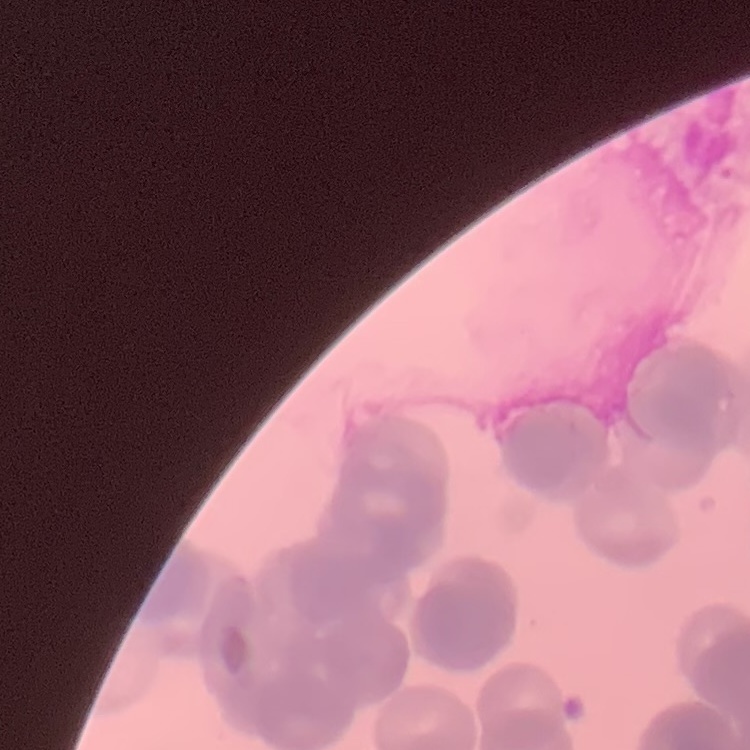
Summary:
  - Erythrocyte morphology: rouleaux formation
  - Stain: Field's or Giemsa
  - Preparation: thin blood film
  - Image type: square crop of a larger photomicrograph